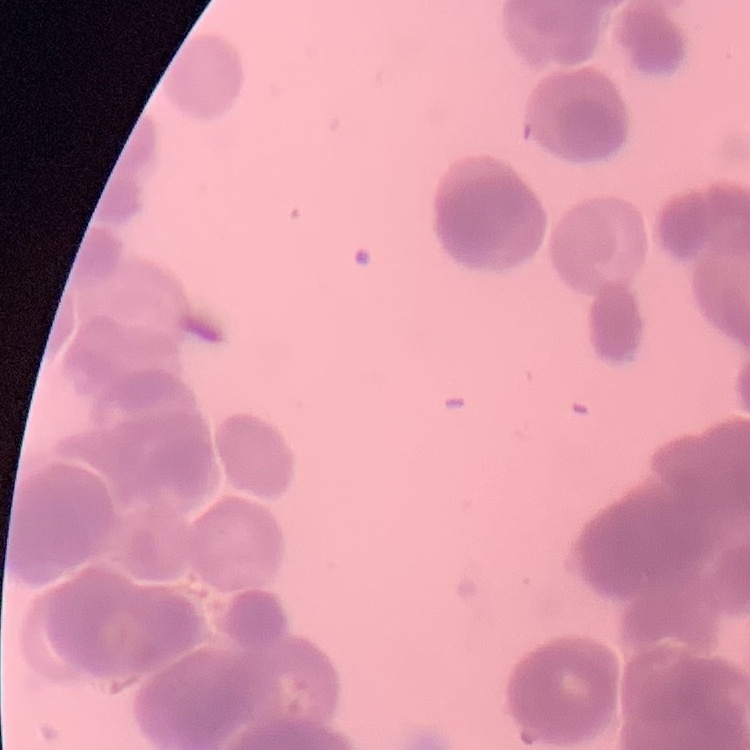
red blood cell morphology = rouleaux formation
preparation = thin blood smear
image type = square crop of a larger photomicrograph
stain = Field's or Giemsa